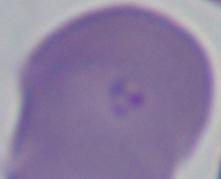

identification: Babesia
magnification: 1000x
modality: micrograph